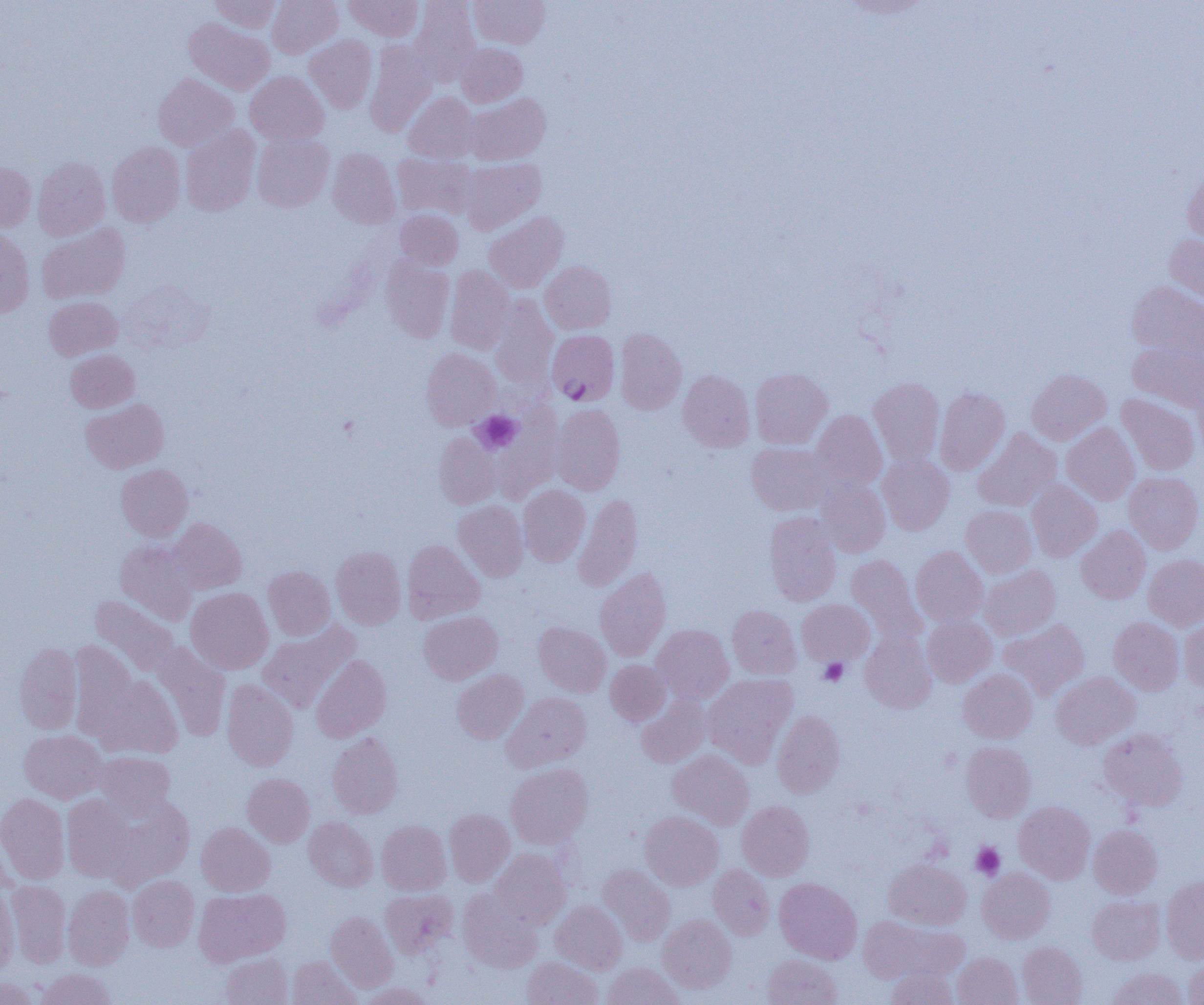
Summary:
  - Coordinate format: approximate bounding boxes as [x1, y1, x2, y2] in pixels
  - Plasmodium falciparum-infected red blood cell locations: [547, 330, 619, 405]
  - Platelet locations: [473, 411, 522, 454], [819, 659, 847, 685], [972, 842, 1005, 879]
  - Uninfected red blood cell locations: [210, 0, 280, 32], [267, 0, 343, 58], [344, 0, 423, 41], [469, 0, 550, 48], [410, 1, 480, 84], [184, 19, 274, 94], [305, 36, 377, 113], [365, 41, 435, 136], [456, 43, 527, 107], [245, 71, 329, 145], [153, 74, 238, 151], [404, 93, 478, 163], [466, 93, 550, 165], [180, 126, 260, 216], [252, 133, 334, 212], [107, 142, 185, 227], [328, 148, 400, 228], [393, 153, 476, 219], [33, 157, 111, 240], [461, 158, 545, 234], [0, 162, 37, 233], [1182, 168, 1204, 247], [396, 210, 462, 269], [484, 212, 568, 293], [37, 223, 130, 304], [0, 230, 34, 317], [1164, 234, 1204, 308], [381, 255, 455, 343], [540, 261, 616, 334], [445, 265, 515, 354], [1127, 281, 1204, 363], [490, 296, 558, 390], [44, 297, 122, 360], [615, 328, 686, 414], [1128, 339, 1204, 412], [421, 349, 500, 429], [65, 350, 139, 413], [750, 368, 833, 449], [678, 369, 755, 452], [1026, 369, 1111, 445], [869, 377, 945, 466], [1194, 381, 1204, 459], [935, 387, 1009, 474], [1117, 394, 1200, 475], [81, 398, 168, 473], [551, 404, 625, 495], [494, 407, 562, 503], [810, 410, 887, 493], [1062, 422, 1139, 505], [973, 428, 1061, 511], [434, 432, 501, 509], [746, 443, 832, 515], [878, 455, 954, 535], [116, 464, 192, 541], [1124, 471, 1204, 554], [817, 480, 890, 557], [1027, 480, 1102, 561], [518, 485, 590, 566], [573, 494, 643, 592], [454, 501, 528, 581], [961, 505, 1036, 577], [765, 512, 841, 606], [169, 518, 246, 593], [1076, 526, 1151, 603], [115, 540, 197, 625], [402, 540, 485, 623], [331, 546, 406, 629], [911, 546, 988, 627], [847, 554, 925, 642], [1143, 554, 1204, 631], [980, 565, 1060, 639], [263, 566, 335, 640], [595, 568, 671, 661], [186, 587, 274, 674], [90, 595, 179, 676], [797, 599, 874, 666], [727, 605, 801, 679], [419, 610, 502, 684], [922, 616, 996, 687], [1179, 616, 1204, 691], [1109, 617, 1184, 694], [999, 619, 1090, 701], [258, 622, 359, 713], [534, 622, 611, 697], [652, 624, 733, 703], [860, 630, 937, 713], [151, 641, 230, 740], [14, 642, 83, 733], [69, 642, 140, 737], [311, 655, 391, 742], [605, 660, 670, 726], [452, 669, 528, 743], [958, 669, 1037, 743], [1051, 671, 1140, 749], [92, 674, 183, 759], [703, 674, 797, 766], [221, 680, 298, 771], [502, 692, 591, 771], [636, 695, 711, 768], [772, 710, 845, 797], [1099, 728, 1188, 810], [19, 729, 107, 803], [327, 731, 403, 818], [961, 742, 1036, 822], [668, 750, 754, 829], [93, 751, 175, 818], [506, 763, 593, 849], [242, 773, 314, 847], [0, 792, 70, 884], [103, 793, 195, 887], [62, 794, 136, 882], [737, 800, 814, 879], [1014, 801, 1095, 883], [444, 808, 515, 886], [640, 811, 723, 889], [304, 816, 378, 891], [377, 820, 451, 895], [197, 823, 275, 896], [1089, 825, 1162, 898], [489, 848, 570, 929], [884, 859, 970, 930], [598, 864, 674, 945], [708, 864, 774, 939], [977, 867, 1054, 943], [128, 875, 199, 951], [1161, 877, 1204, 963], [774, 878, 862, 963], [6, 880, 71, 967], [0, 885, 18, 974], [63, 885, 134, 970], [194, 887, 290, 966], [380, 889, 457, 959], [457, 890, 542, 972], [1088, 895, 1164, 965], [550, 901, 627, 974], [326, 911, 398, 992], [658, 914, 736, 993], [856, 917, 961, 984], [1017, 941, 1087, 1005], [952, 952, 1022, 1005], [220, 953, 292, 1005], [762, 954, 841, 1005], [522, 956, 602, 1005], [1183, 956, 1204, 1005], [287, 957, 361, 1005], [602, 962, 684, 1005], [886, 967, 957, 1004], [36, 968, 115, 1005], [1108, 968, 1188, 1005], [0, 976, 41, 1004], [360, 983, 433, 1005]
  - Slide-level diagnosis: Plasmodium falciparum
  - Field of view: single
  - Modality: optical microscopy
  - Image size: 1204×1005 pixels
  - Preparation: thin blood film
  - Magnification: 1000x